Assess this cell for malaria.
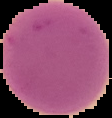

It is uninfected.

image type = segmented cell region with the area outside set to black
preparation = thin blood film
image size = 112×118 pixels